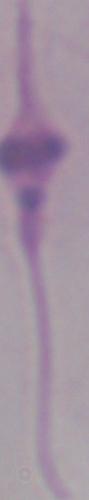
identification = Leishmania
modality = micrograph
magnification = 1000x